Identify the parasite.
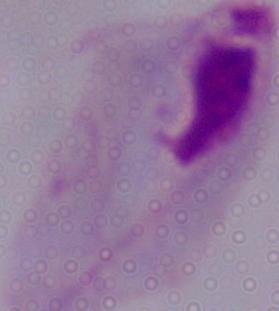
A trichomonad.

modality = photomicrograph
magnification = 1000x